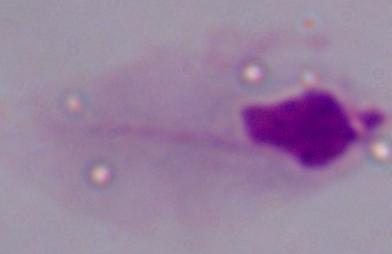

magnification = 1000x
modality = micrograph
identification = trichomonad